Assess this cell for malaria.
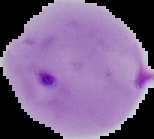

It is parasitized.

Summary:
  - Image type: segmented cell region with the area outside set to black
  - Preparation: thin blood film
  - Image size: 154×139 pixels